Comment on the morphology of the red blood cells.
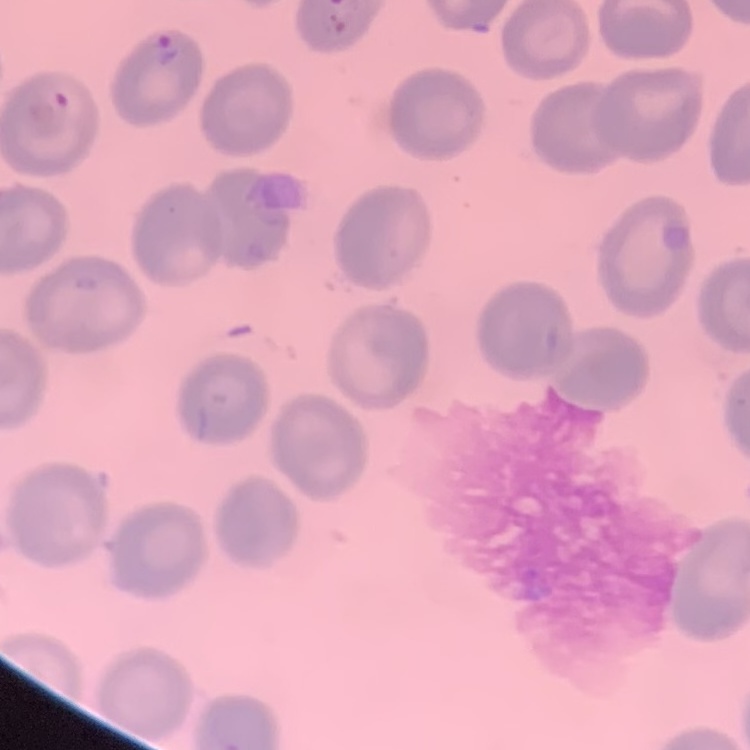

They show no rouleaux formation.

image type = one tile cut from a larger photomicrograph
preparation = thin peripheral smear
stain = Field's or Giemsa